Point out each Plasmodium parasite.
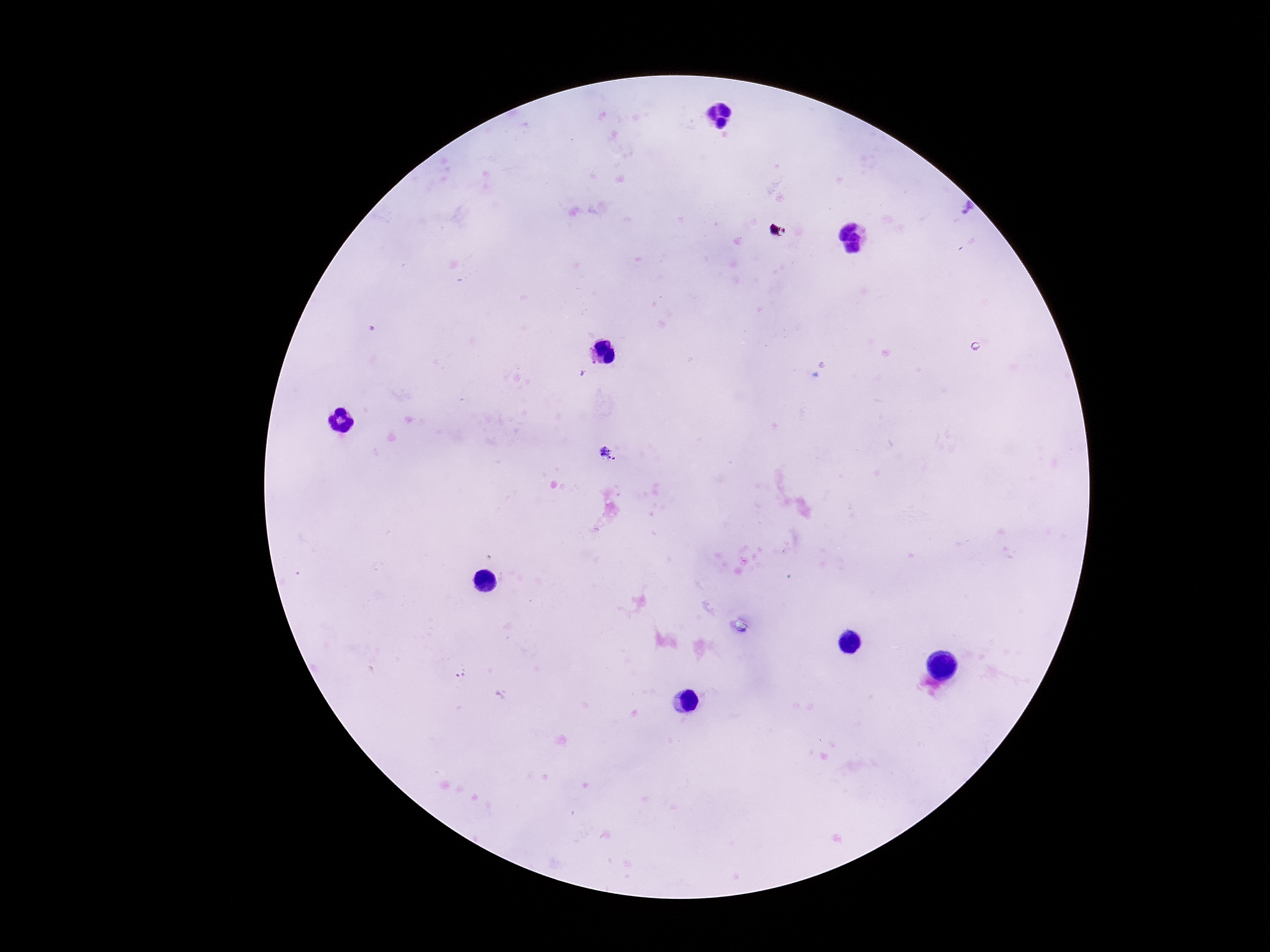
Approximate centers as {x, y} in pixels.
Plasmodium parasites: {777, 231}, {609, 455}.

Summary:
  - Stain: Giemsa
  - Field of view: single
  - Capture: smartphone camera through the microscope eyepiece
  - Preparation: thick blood smear
  - Magnification: 100x
  - Image size: 1270×952 pixels
  - Patient malaria status: infected